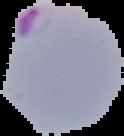 Image is 124×136 pixels. Malaria status: parasitized. The area outside the segmented cell region is set to black. From a thin blood smear.